Point out each malaria parasite.
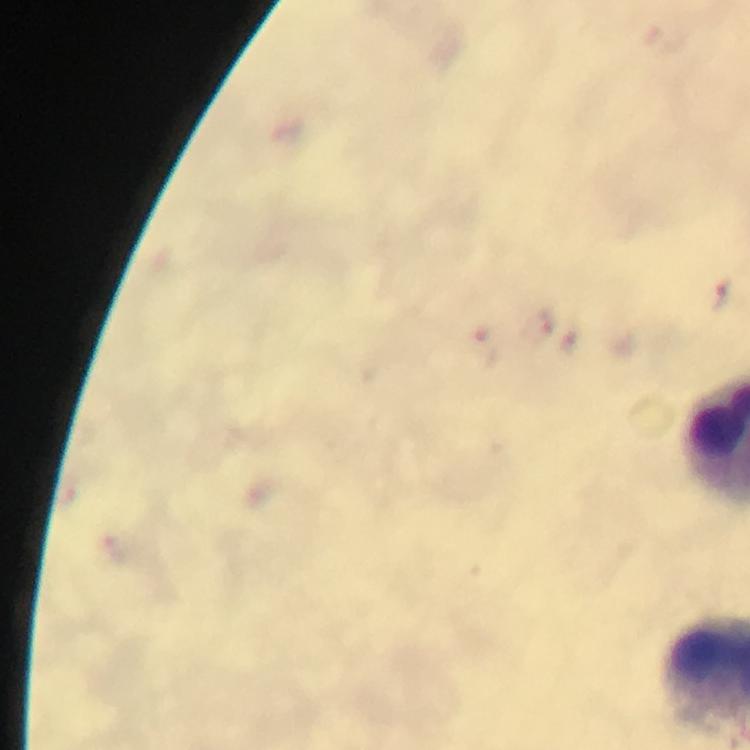

Approximate centers as (x, y) in pixels.
Malaria parasites: (725, 296).

context: from a malaria diagnostic workup
magnification: 100x
immersion_oil: applied
stain: Giemsa
image_size: 750×750 pixels
capture: smartphone mounted on the microscope
cropped_from: a single field of view
preparation: thick smear